Give the position of every Plasmodium parasite visible.
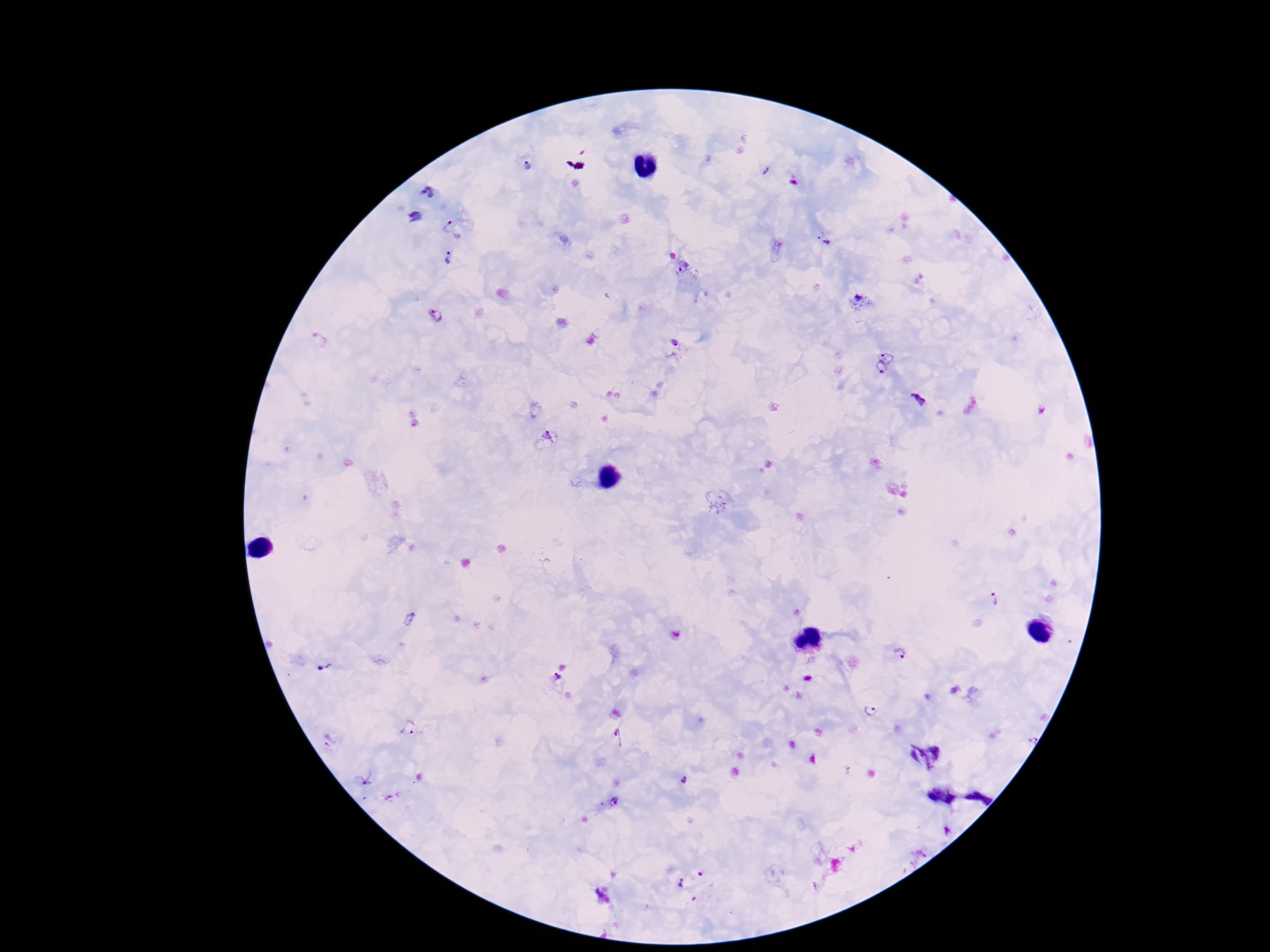

Approximate centers as (x, y) in pixels.
Plasmodium parasites: (528, 166), (765, 170), (428, 193), (416, 217), (455, 228), (819, 234), (828, 242), (447, 258), (685, 268), (859, 301), (436, 316), (676, 343), (890, 353), (876, 371), (918, 399), (547, 438), (992, 600), (897, 654), (323, 668), (555, 678), (869, 711), (409, 728), (619, 738), (328, 742), (365, 779), (683, 780), (615, 802), (682, 882).

Image is 1270×952 pixels. Thick peripheral-blood smear. 100x magnification. Single field of view. Photographed through the microscope eyepiece with a smartphone camera. Giemsa stain. Patient malaria status: infected.